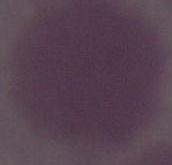
Summary:
  - Identification: red blood cell
  - Magnification: 1000x
  - Modality: micrograph